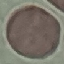
malaria status = uninfected
stain = Giemsa
preparation = thin smear
image type = cell patch, automatically extracted from a larger field of view and resized to 64 × 64 pixels
capture = smartphone camera at the microscope eyepiece